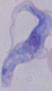

Summary:
  - Identification: trypanosome
  - Magnification: 1000x
  - Modality: micrograph